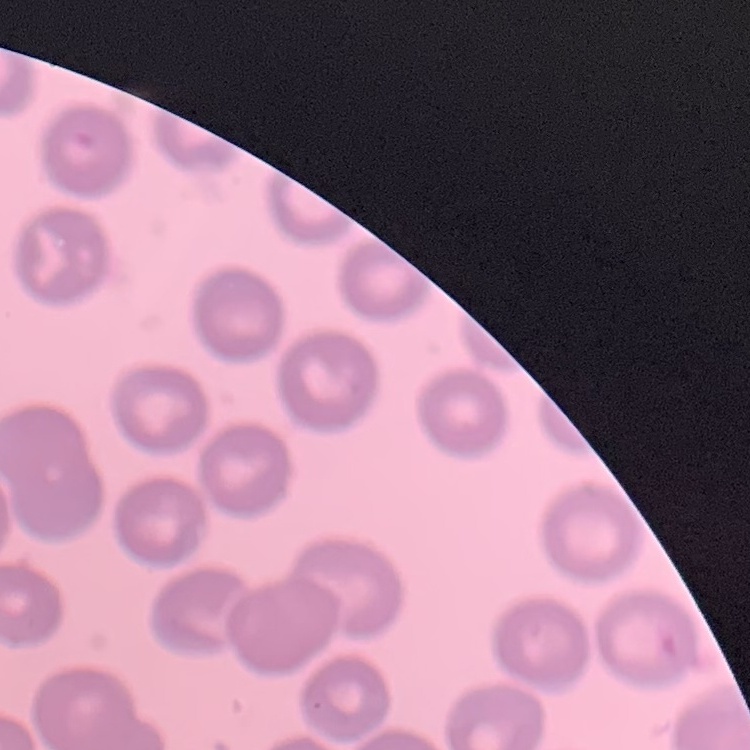 The red blood cells exhibit no rouleaux formation. One tile cut from a larger photomicrograph. Thin blood smear. Stained with either Field's or Giemsa.